Assess the morphology of the erythrocytes.
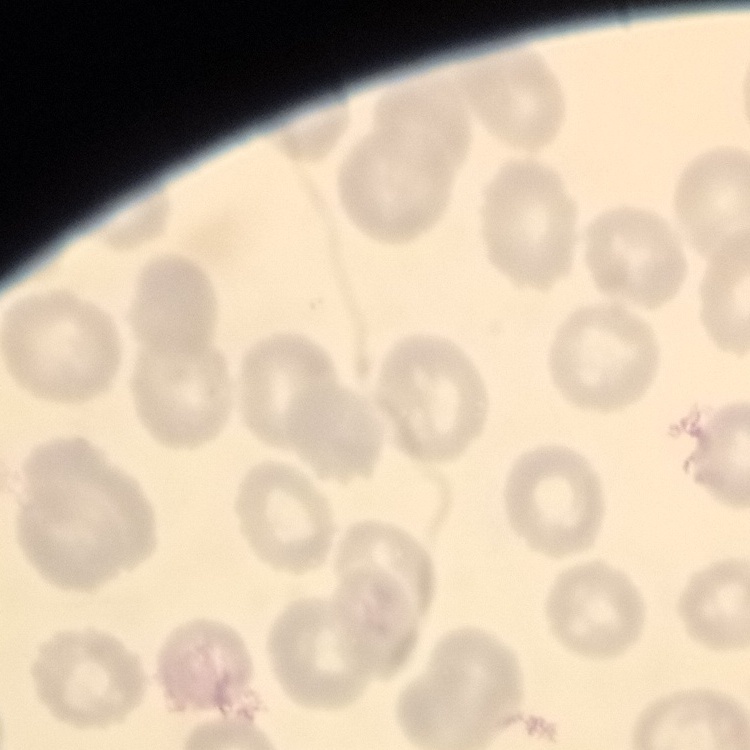
They show no rouleaux formation.

Thin blood film. Stained with either Field's or Giemsa. One tile cut from a larger photomicrograph.